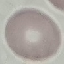 Result: no malaria parasites detected. Cell patch, automatically extracted from a larger field of view and resized to 64 × 64 pixels. Giemsa-stained preparation. Thin smear of blood. Photographed with a smartphone camera at the microscope eyepiece.